Describe the morphology of the red blood cells.
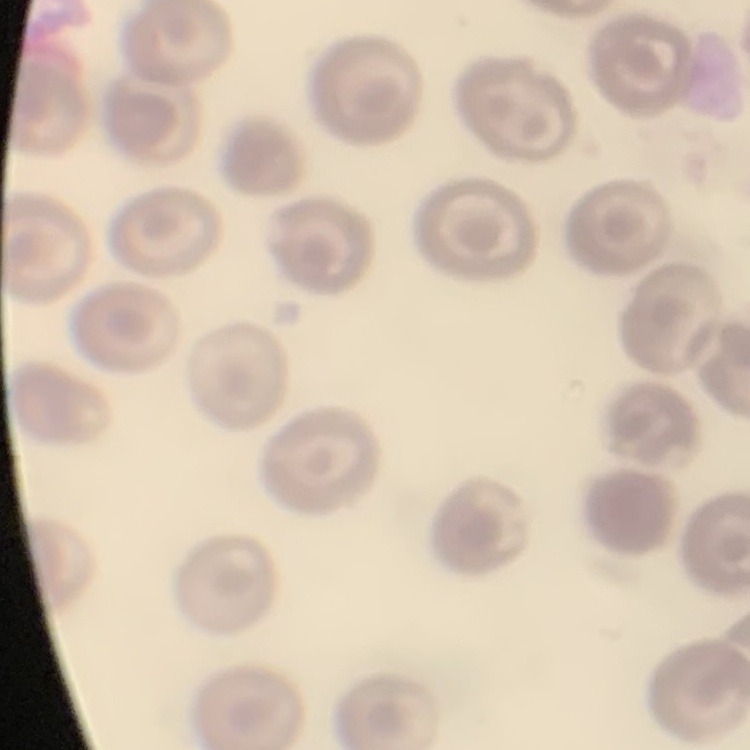
They show no rouleaux formation.

Summary:
  - Stain: Field's or Giemsa
  - Image type: square crop of a larger photomicrograph
  - Preparation: thin blood film